Assess the morphology of the red blood cells.
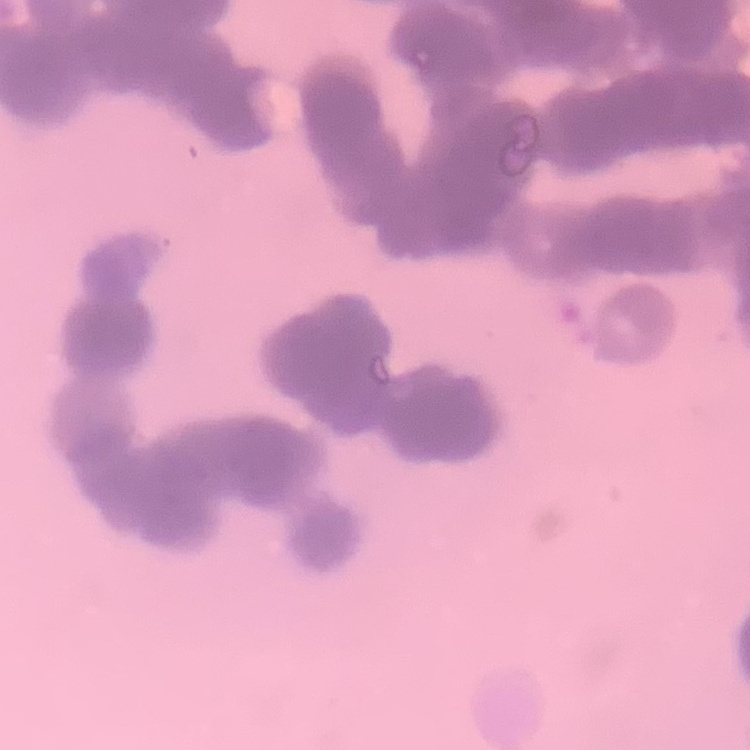
They show rouleaux formation.

preparation = thin blood smear
stain = Field's or Giemsa
image type = one tile cut from a larger photomicrograph